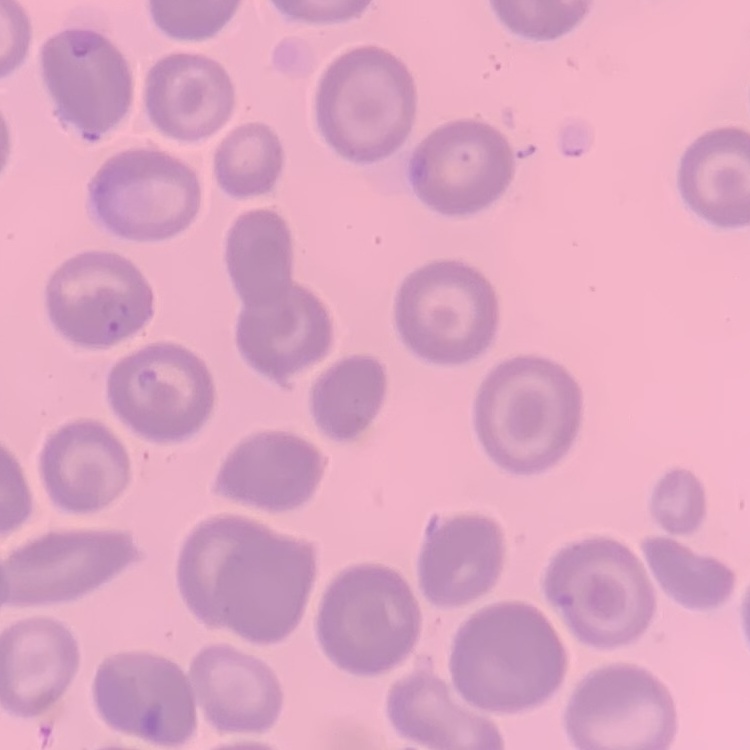
red blood cell morphology = no rouleaux formation
image type = square crop of a larger photomicrograph
preparation = thin peripheral smear
stain = Field's or Giemsa